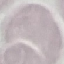 Result: no malaria parasites seen. Photographed with a smartphone camera at the microscope eyepiece. Giemsa-stained preparation. Thin blood film. Automatically extracted cell patch, resized to 64 × 64 pixels.